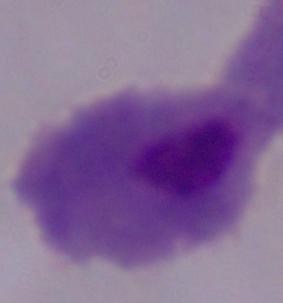
Micrograph. A trichomonad is seen. 1000x magnification.